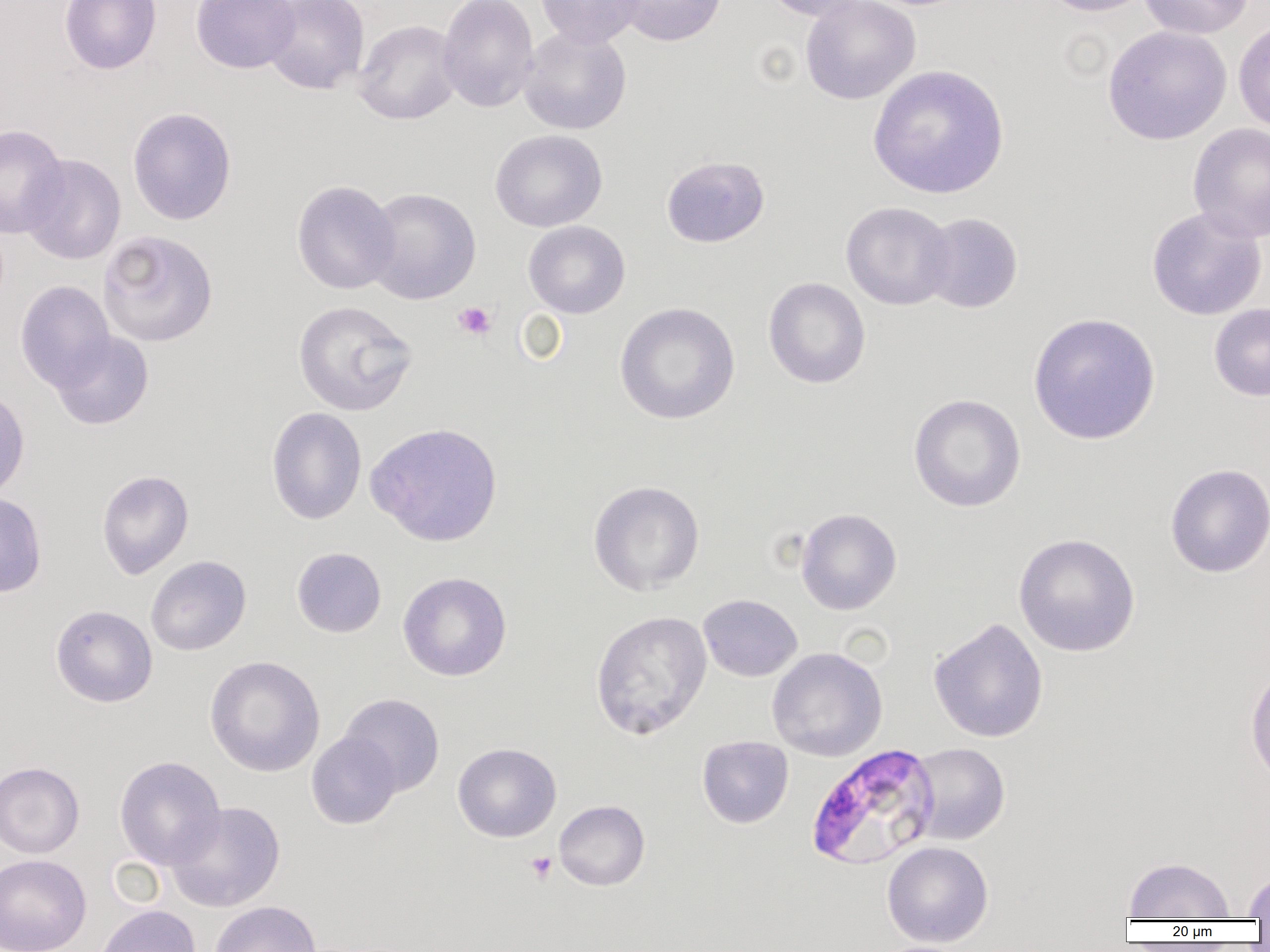

Summary:
  - Coordinate format: approximate bounding boxes as (x1, y1, x2, y2) in pixels
  - Uninfected red blood cell locations: (59, 0, 161, 74), (191, 0, 300, 74), (262, 0, 369, 95), (437, 0, 539, 113), (535, 0, 643, 48), (612, 0, 727, 46), (762, 0, 879, 22), (800, 0, 921, 104), (1040, 0, 1156, 17), (1138, 0, 1254, 39), (1233, 18, 1270, 134), (353, 19, 463, 125), (1102, 25, 1232, 146), (518, 27, 632, 134), (867, 64, 1010, 199), (127, 107, 237, 225), (1187, 123, 1270, 242), (0, 124, 69, 238), (489, 129, 607, 232), (20, 154, 126, 265), (661, 155, 770, 248), (291, 180, 401, 295), (364, 187, 482, 304), (840, 201, 955, 310), (1146, 207, 1267, 321), (918, 212, 1023, 313), (523, 221, 630, 318), (97, 230, 218, 347), (763, 277, 870, 389), (15, 280, 116, 392), (292, 300, 418, 416), (614, 302, 740, 425), (1209, 303, 1270, 401), (1027, 312, 1161, 445), (50, 330, 154, 430), (0, 385, 30, 503), (908, 393, 1027, 513), (266, 407, 367, 525), (366, 421, 502, 547), (1166, 463, 1270, 578), (96, 469, 194, 579), (588, 480, 705, 595), (0, 491, 48, 598), (795, 508, 902, 615), (1014, 533, 1140, 657), (291, 547, 386, 638), (146, 555, 251, 656), (398, 572, 512, 681), (697, 594, 802, 682), (50, 605, 157, 707), (590, 611, 712, 740), (928, 618, 1049, 743), (767, 648, 888, 762), (204, 655, 325, 777), (1244, 667, 1270, 787), (339, 693, 445, 797), (306, 732, 401, 830), (697, 736, 793, 828), (907, 742, 1010, 845), (453, 743, 561, 842), (114, 756, 226, 870), (0, 761, 85, 858), (554, 800, 650, 891), (166, 801, 286, 912), (882, 841, 993, 947), (0, 853, 91, 952), (1123, 856, 1235, 920), (1243, 870, 1270, 918), (209, 900, 321, 952), (94, 904, 201, 952)
  - Plasmodium falciparum-infected red blood cell locations: (806, 743, 941, 871)
  - Platelet locations: (453, 301, 496, 340), (526, 851, 557, 884)
  - Slide-level diagnosis: Plasmodium falciparum
  - Image size: 1270×952 pixels
  - Field of view: one of a larger specimen
  - Modality: optical microscopy
  - Preparation: thin blood film
  - Magnification: 1000x